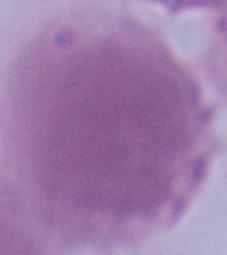
1000x magnification. An erythrocyte is seen. Micrograph.